Report the malaria status of this cell.
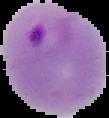
It is parasitized.

preparation = thin blood film
image type = cell region segmented out of the field of view; surrounding area masked to black
image size = 109×118 pixels